Identify the cell.
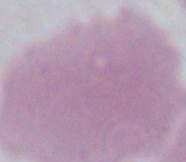
This is an erythrocyte.

Captured at 1000x magnification. Photomicrograph.